Report the malaria status of this cell.
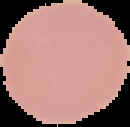
Uninfected.

Summary:
  - Image type: segmented cell region with the area outside set to black
  - Preparation: thin blood smear
  - Image size: 130×127 pixels